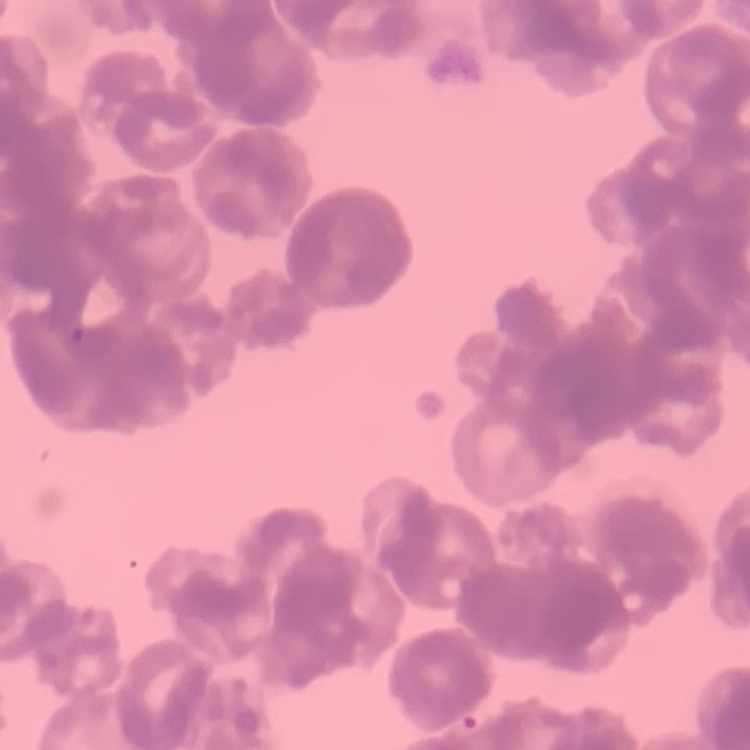 The erythrocytes exhibit rouleaux formation. Square crop of a larger photomicrograph. Thin peripheral smear. Field's or Giemsa stain.